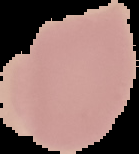
Summary:
  - Preparation: thin blood film
  - Result: negative for Plasmodium parasites
  - Image size: 139×154 pixels
  - Image type: cell region segmented out of the field of view; surrounding area masked to black